Give the position of every Plasmodium parasite.
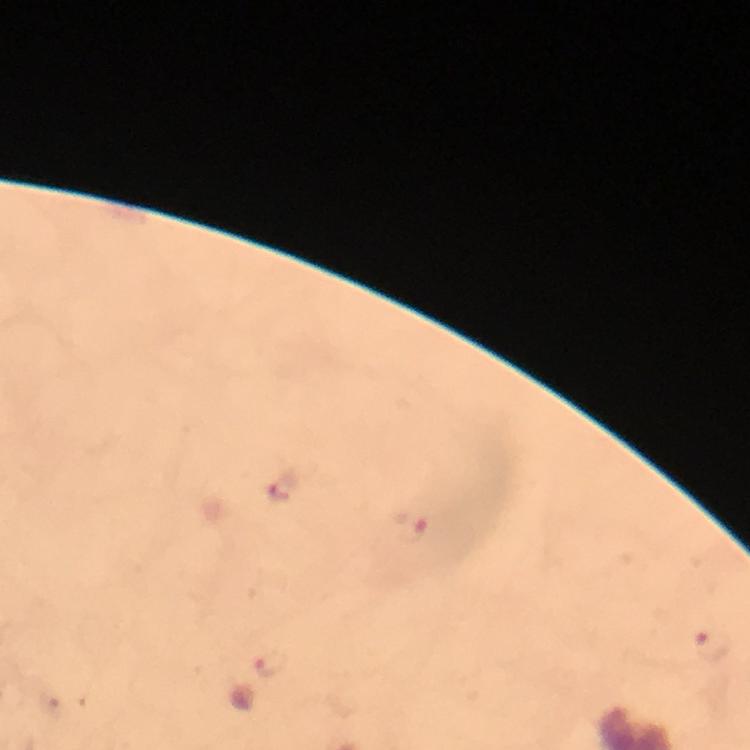
Approximate centers as [x, y] in pixels.
Plasmodium parasites: [283, 496], [411, 527], [714, 644], [270, 666].

Summary:
  - Magnification: 100x
  - Context: from a diagnostic examination for malaria
  - Preparation: thick blood film
  - Stain: Giemsa
  - Image size: 750×750 pixels
  - Capture: smartphone camera through the microscope
  - Immersion oil: applied
  - Cropped from: one field of view